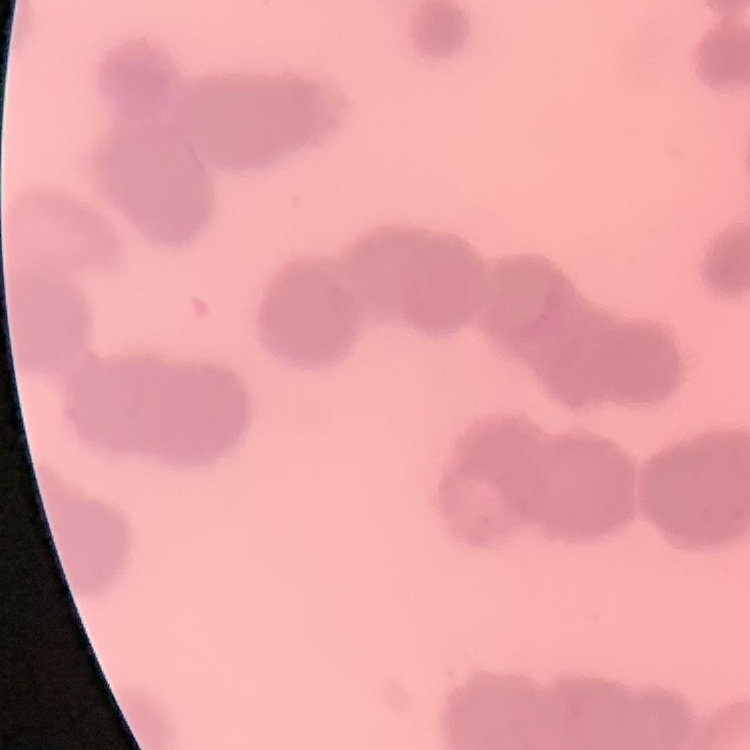
erythrocyte morphology = rouleaux formation
image type = square crop of a larger photomicrograph
preparation = thin peripheral smear
stain = Field's or Giemsa